Locate every malaria parasite.
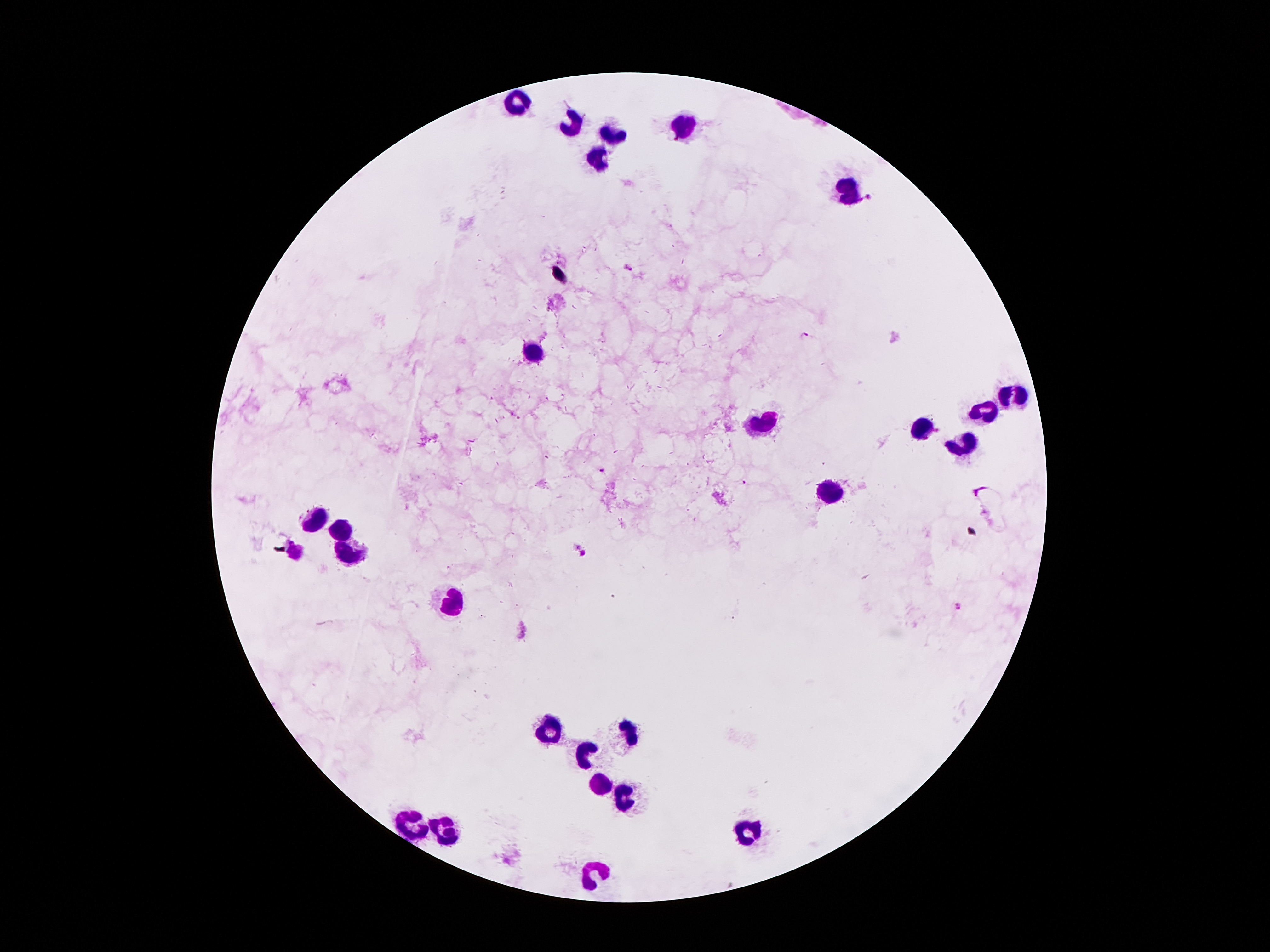

Approximate object centers, in pixels from the top-left corner.
Malaria parasites: (x=870, y=196), (x=627, y=266), (x=808, y=336), (x=604, y=469), (x=743, y=481), (x=585, y=554), (x=962, y=606).

Leukocyte locations: (x=519, y=100), (x=569, y=122), (x=679, y=129), (x=615, y=134), (x=595, y=158), (x=848, y=187), (x=533, y=352), (x=1013, y=393), (x=987, y=407), (x=763, y=422), (x=922, y=429), (x=965, y=443), (x=828, y=491), (x=315, y=520), (x=343, y=527), (x=298, y=551), (x=346, y=557), (x=454, y=605), (x=550, y=726), (x=629, y=731), (x=586, y=750), (x=603, y=784), (x=624, y=801), (x=411, y=825), (x=442, y=825), (x=754, y=827), (x=593, y=876). Thick blood film. Image is 1270×952 pixels. Photographed through the microscope eyepiece with a smartphone camera. Giemsa-stained preparation. Patient malaria status: infected with Plasmodium falciparum. Single field of view. 100x magnification.